Describe the morphology of the red blood cells.
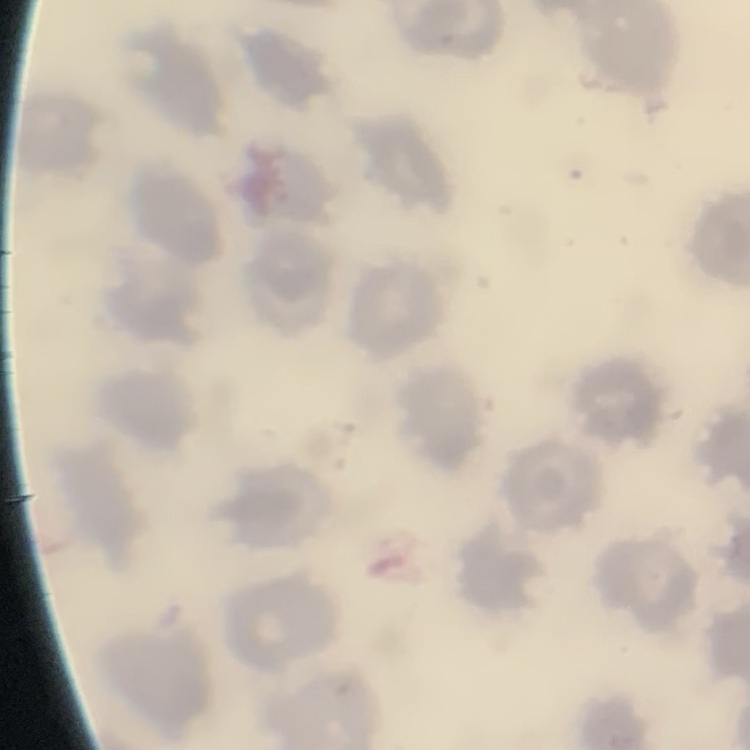
No rouleaux formation.

Summary:
  - Stain: Field's or Giemsa
  - Image type: one tile cut from a larger photomicrograph
  - Preparation: thin peripheral smear